Locate every Plasmodium parasite.
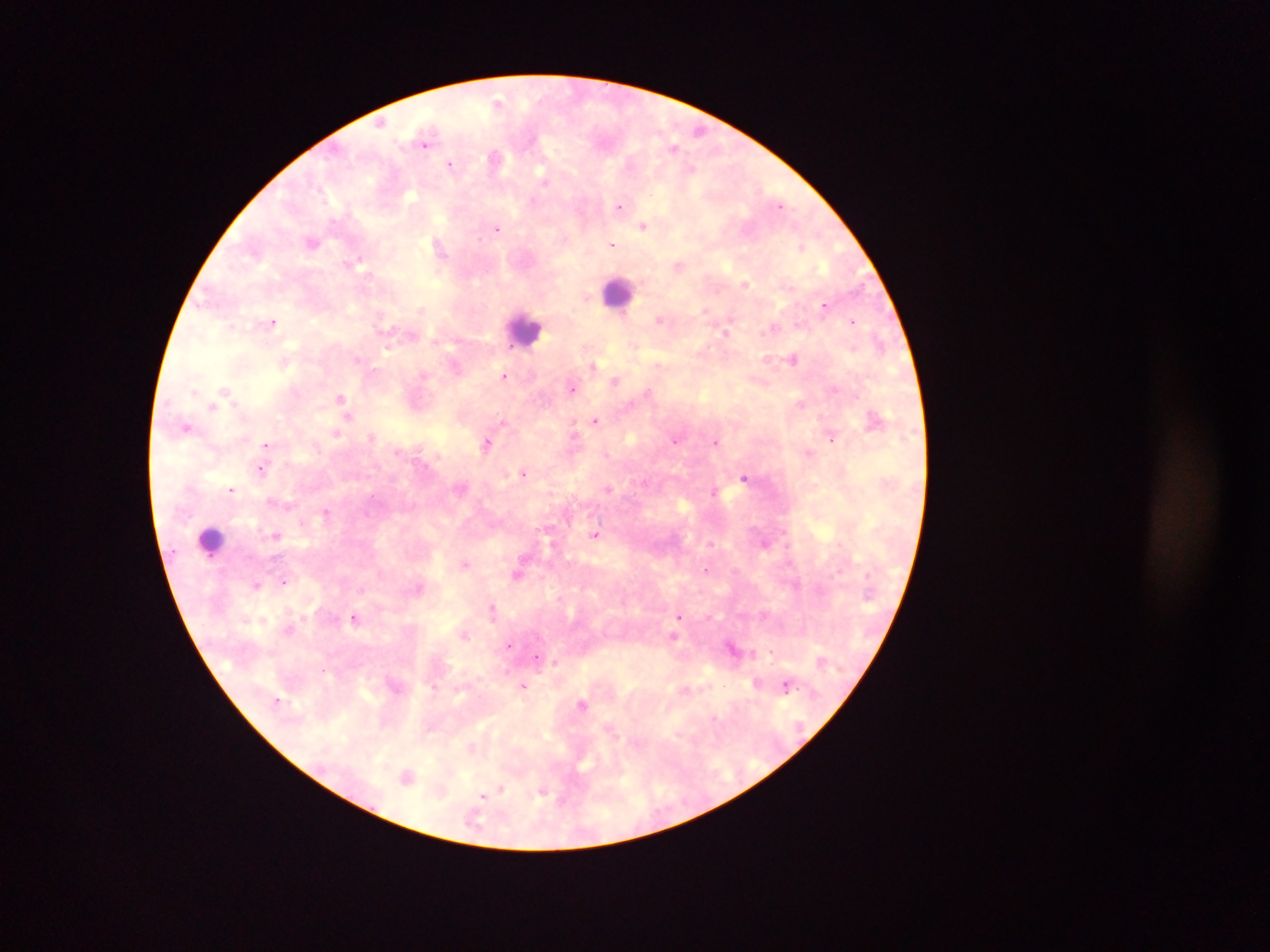

Approximate centers as x y in pixels.
Plasmodium parasites: 499 103; 380 123; 699 129; 425 144; 674 148; 496 158; 451 164; 691 169; 544 177; 532 202; 779 205; 619 207; 643 225; 497 229; 312 242; 613 245; 802 247; 359 258; 679 266; 745 284; 587 297; 824 305; 421 310; 705 310; 658 318; 853 321; 272 323; 772 329; 725 333; 386 348; 357 360; 794 360; 657 365; 594 366; 504 376; 615 381; 572 388; 224 390; 648 392; 340 398; 801 403; 212 406; 348 417; 595 420; 186 427; 573 431; 337 433; 372 436; 832 438; 675 441; 715 442; 487 443; 266 446; 808 453; 261 469; 523 473; 744 478; 232 490; 608 490; 713 491; 326 512; 276 535; 595 535; 466 563; 706 570; 518 575; 284 582; 256 584; 419 588; 492 608; 679 616; 354 617; 465 635; 673 636; 509 645; 771 652; 537 657; 554 662; 757 683; 523 686; 786 686; 582 703; 715 717; 407 777; 500 789; 542 793; 483 796.

Summary:
  - Leukocyte locations: 619 293; 526 330; 211 541
  - Country: Ghana
  - Image size: 1270×952 pixels
  - Field of view: single
  - Preparation: thick blood smear
  - Capture: mobile-phone photograph through a microscope